Name the cell type shown.
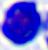

This is a leukocyte.

Captured at 400x magnification. Micrograph.